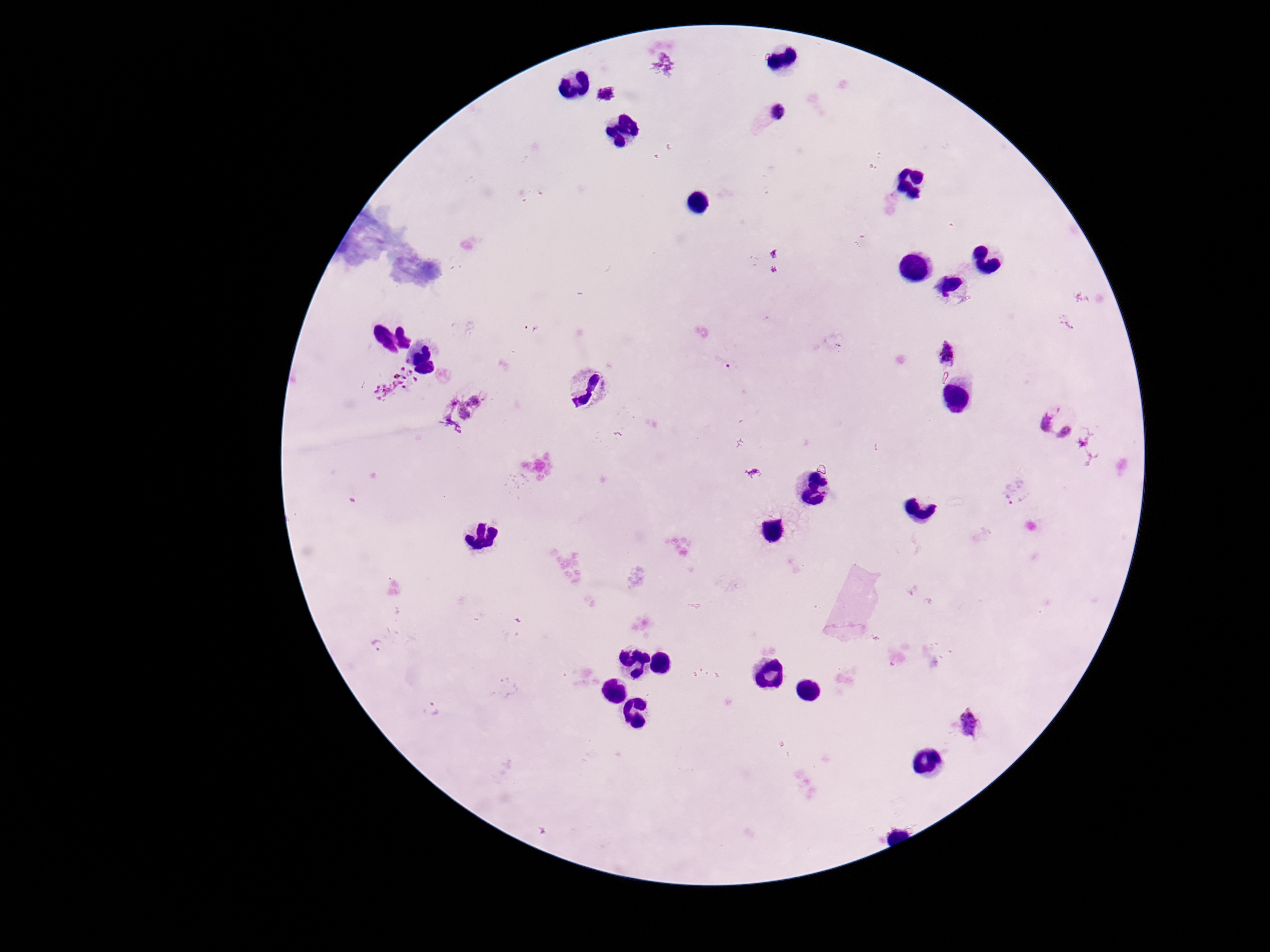
Approximate centers as (x, y) in pixels.
Summary:
  - Plasmodium parasite locations: (607, 96), (767, 116), (946, 353), (395, 383), (472, 408), (1058, 421), (1015, 492), (378, 646), (431, 709), (968, 724)
  - Image size: 1270×952 pixels
  - Capture: smartphone camera through the microscope eyepiece
  - Field of view: single
  - Patient malaria status: positive
  - Stain: Giemsa
  - Preparation: thick blood smear
  - Magnification: 100x